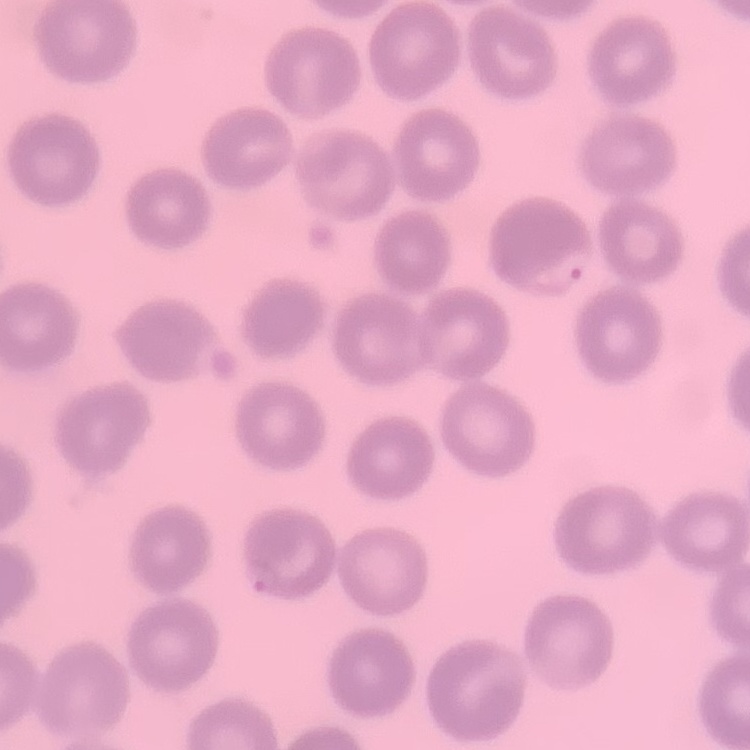

{
  "red_blood_cell_morphology": "no rouleaux formation",
  "preparation": "thin blood smear",
  "stain": "Field's or Giemsa",
  "image_type": "square crop of a larger photomicrograph"
}